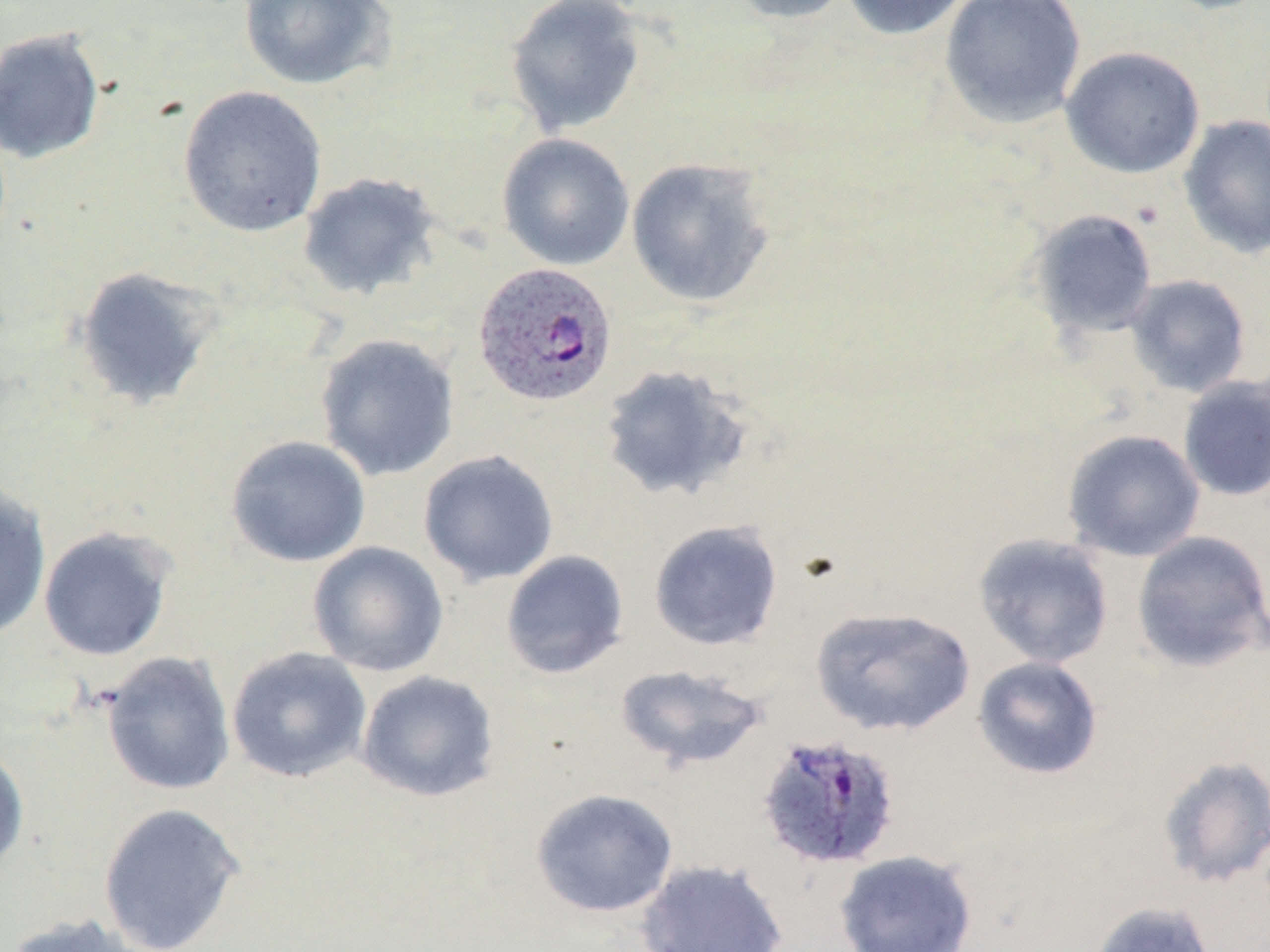

slide_level_diagnosis: Plasmodium ovale
field_of_view: one of a larger specimen
stain: May-Grünwald-Giemsa
plasmodium_ovale_infected_red_blood_cell_locations: 'approximate bounding boxes as [x1, y1, x2, y2] in pixels: [472, 262, 617, 407], [755, 733, 902, 871]'
image_size: 1270×952 pixels
uninfected_red_blood_cell_locations: 'approximate bounding boxes as [x1, y1, x2, y2] in pixels: [237, 0, 397, 91], [728, 0, 854, 24], [840, 0, 973, 41], [939, 0, 1087, 129], [1155, 0, 1270, 14], [504, 1, 647, 136], [0, 27, 106, 165], [1060, 45, 1205, 179], [176, 85, 328, 237], [1178, 115, 1270, 259], [497, 133, 635, 270], [625, 157, 778, 309], [297, 172, 442, 301], [1028, 208, 1158, 339], [73, 265, 223, 411], [1125, 274, 1252, 397], [315, 333, 460, 481], [598, 363, 755, 504], [1178, 376, 1270, 502], [1062, 429, 1205, 562], [225, 435, 372, 568], [417, 450, 559, 587], [0, 480, 52, 643], [648, 520, 784, 651], [38, 525, 175, 662], [1131, 530, 1270, 672], [973, 532, 1114, 669], [307, 541, 449, 677], [501, 550, 629, 679], [810, 606, 975, 737], [226, 646, 372, 784], [100, 651, 236, 796], [972, 655, 1104, 780], [614, 663, 768, 771], [355, 669, 500, 803], [0, 743, 30, 875], [1156, 755, 1270, 889], [530, 788, 679, 918], [96, 800, 247, 952], [833, 849, 978, 952], [635, 858, 789, 952], [1088, 901, 1218, 952], [3, 912, 150, 952]'
magnification: 1000x
preparation: thin blood film
modality: light microscopy